Assess the morphology of the erythrocytes.
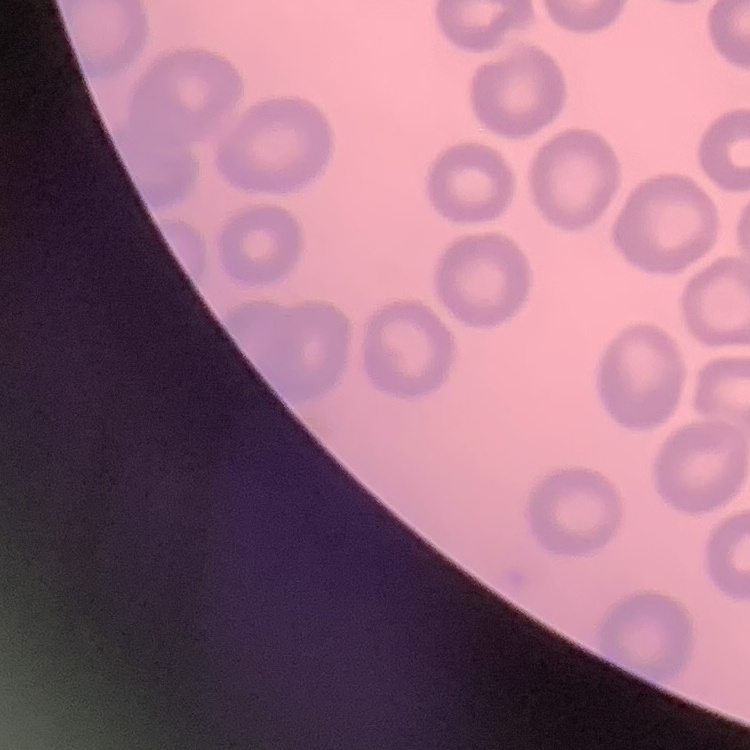

No rouleaux formation.

Summary:
  - Preparation: thin blood film
  - Image type: one tile cut from a larger photomicrograph
  - Stain: Field's or Giemsa